Name the cell type shown.
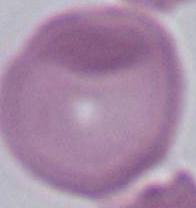

An erythrocyte.

Summary:
  - Magnification: 1000x
  - Modality: photomicrograph